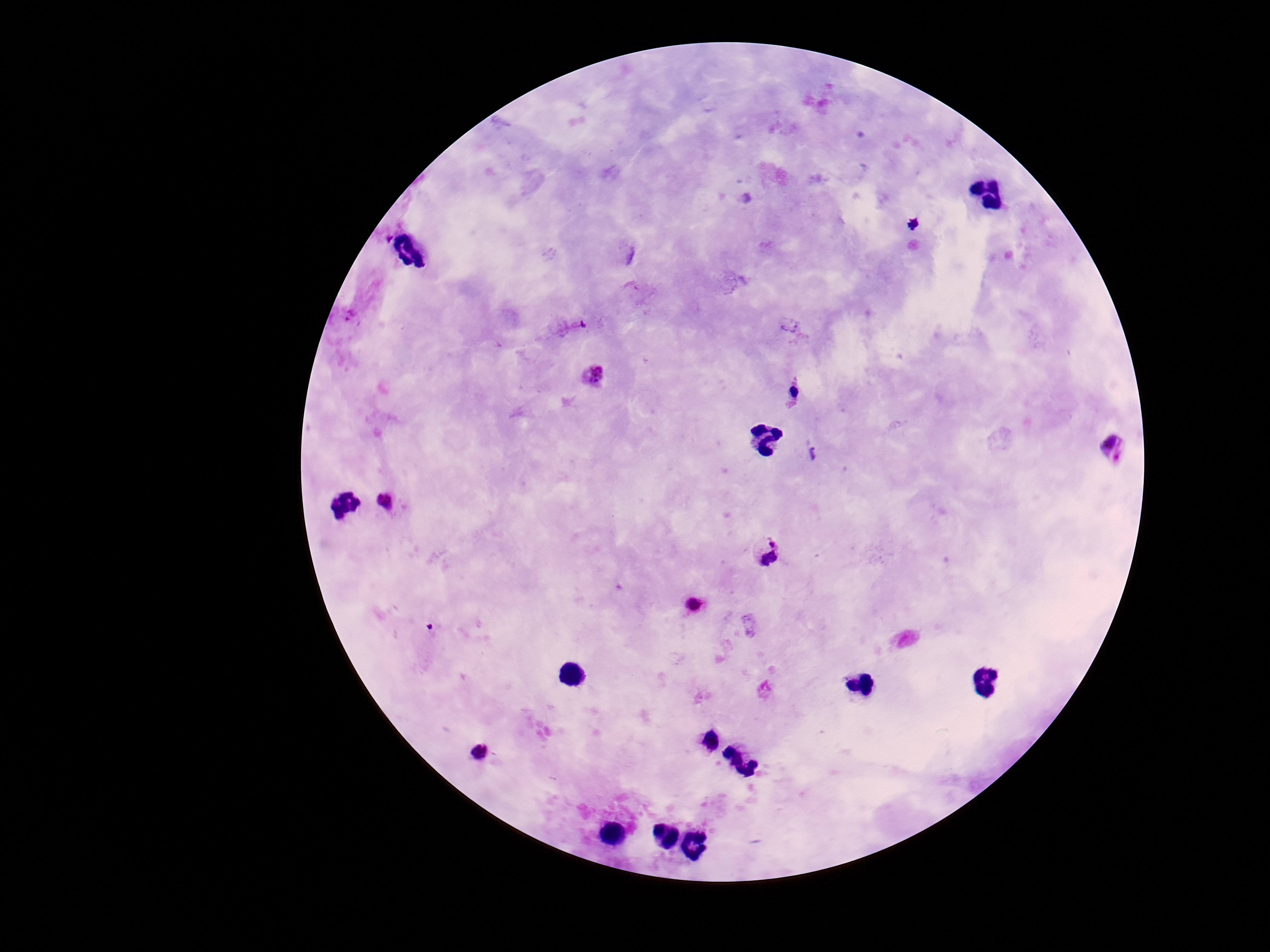

Approximate centers as {x, y} in pixels.
Summary:
  - Plasmodium parasite locations: {914, 224}, {594, 375}, {794, 392}, {1113, 446}, {812, 454}, {387, 503}, {767, 549}, {695, 603}, {478, 753}
  - Image size: 1270×952 pixels
  - Magnification: 100x
  - Preparation: thick blood smear
  - Patient malaria status: infected
  - Stain: Giemsa
  - Field of view: one from this slide
  - Capture: smartphone camera through the microscope eyepiece